Assess this cell for malaria.
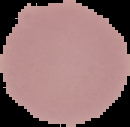
Uninfected.

image size = 130×127 pixels
image type = segmented cell region with the area outside set to black
preparation = thin blood smear